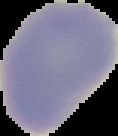

Summary:
  - Image size: 118×136 pixels
  - Result: negative for malaria parasites
  - Image type: cell region segmented out of the field of view; surrounding area masked to black
  - Preparation: thin blood smear